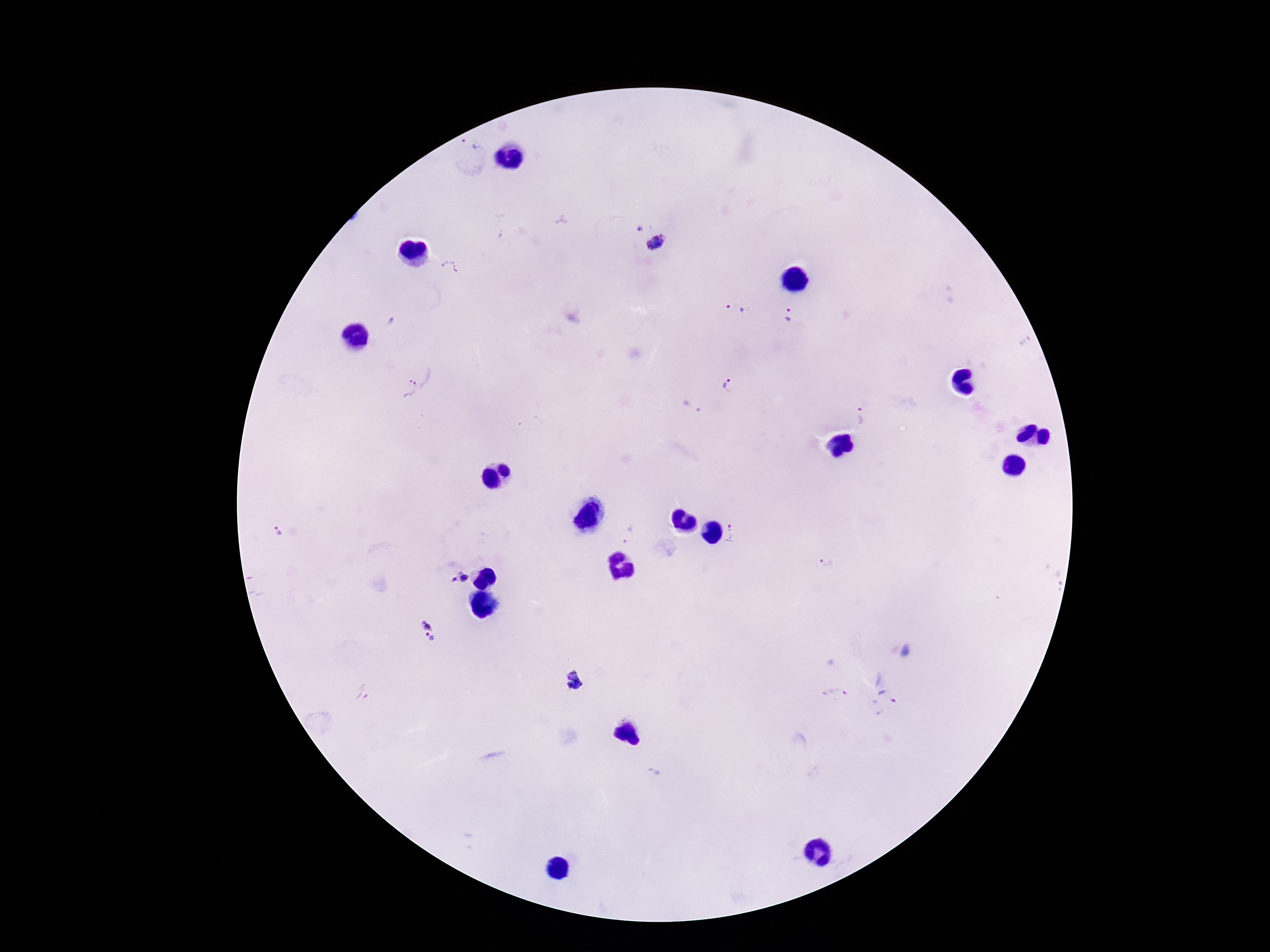

image size = 1270×952 pixels
Plasmodium parasite locations = approximate centers as (x, y) in pixels: (470, 142), (638, 230), (656, 242), (451, 268), (735, 309), (791, 315), (392, 322), (729, 384), (409, 387), (691, 406), (861, 416), (628, 533), (278, 534), (736, 534), (826, 564), (456, 578), (428, 631), (574, 680), (362, 692), (836, 694), (886, 698), (654, 773)
preparation = thick blood smear
capture = smartphone camera through the microscope eyepiece
field of view = single
patient malaria status = positive
magnification = 100x
stain = Giemsa